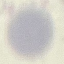

Summary:
  - Malaria status: uninfected
  - Capture: smartphone through the microscope eyepiece
  - Preparation: thin smear
  - Image type: cell patch, automatically extracted from a larger field of view and resized to 64 × 64 pixels
  - Stain: Giemsa